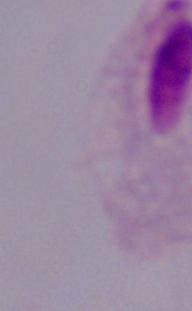
1000x magnification. A trichomonad is shown. Photomicrograph.